Identify the parasite.
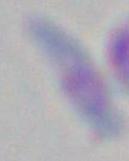
Toxoplasma gondii.

1000x magnification. Photomicrograph.